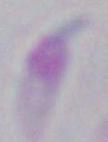
modality: photomicrograph
identification: Toxoplasma gondii
magnification: 1000x